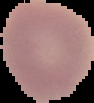 Segmented cell region on a black background. From a thin blood smear. Image is 94×103 pixels. Malaria status: uninfected.